Locate every malaria parasite.
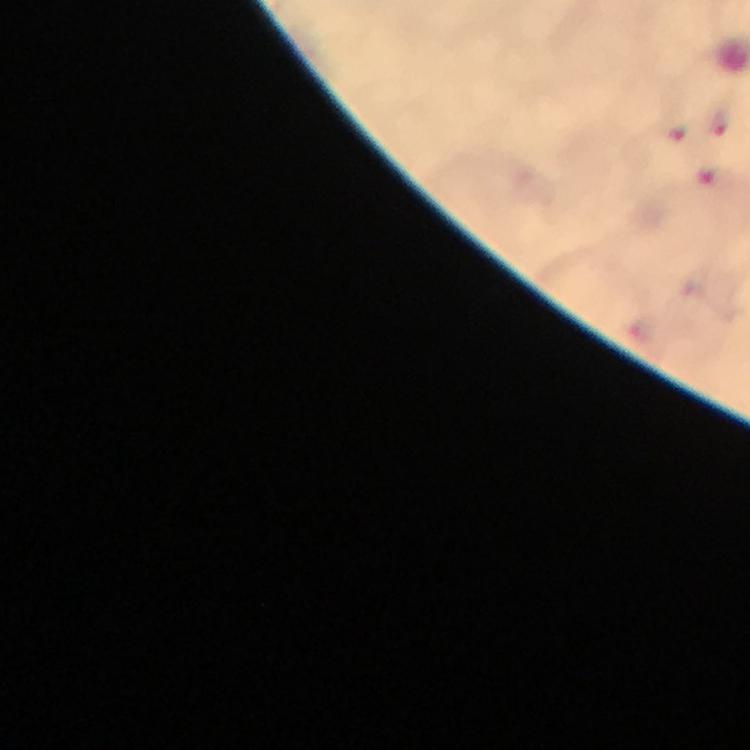

Approximate centers as {x, y} in pixels.
Malaria parasites: {720, 126}, {676, 133}, {712, 179}.

Summary:
  - Context: from a malaria diagnostic workup
  - Image size: 750×750 pixels
  - Magnification: 100x
  - Preparation: thick smear
  - Stain: Giemsa
  - Immersion oil: applied
  - Cropped from: a single field of view
  - Capture: smartphone photograph through a microscope